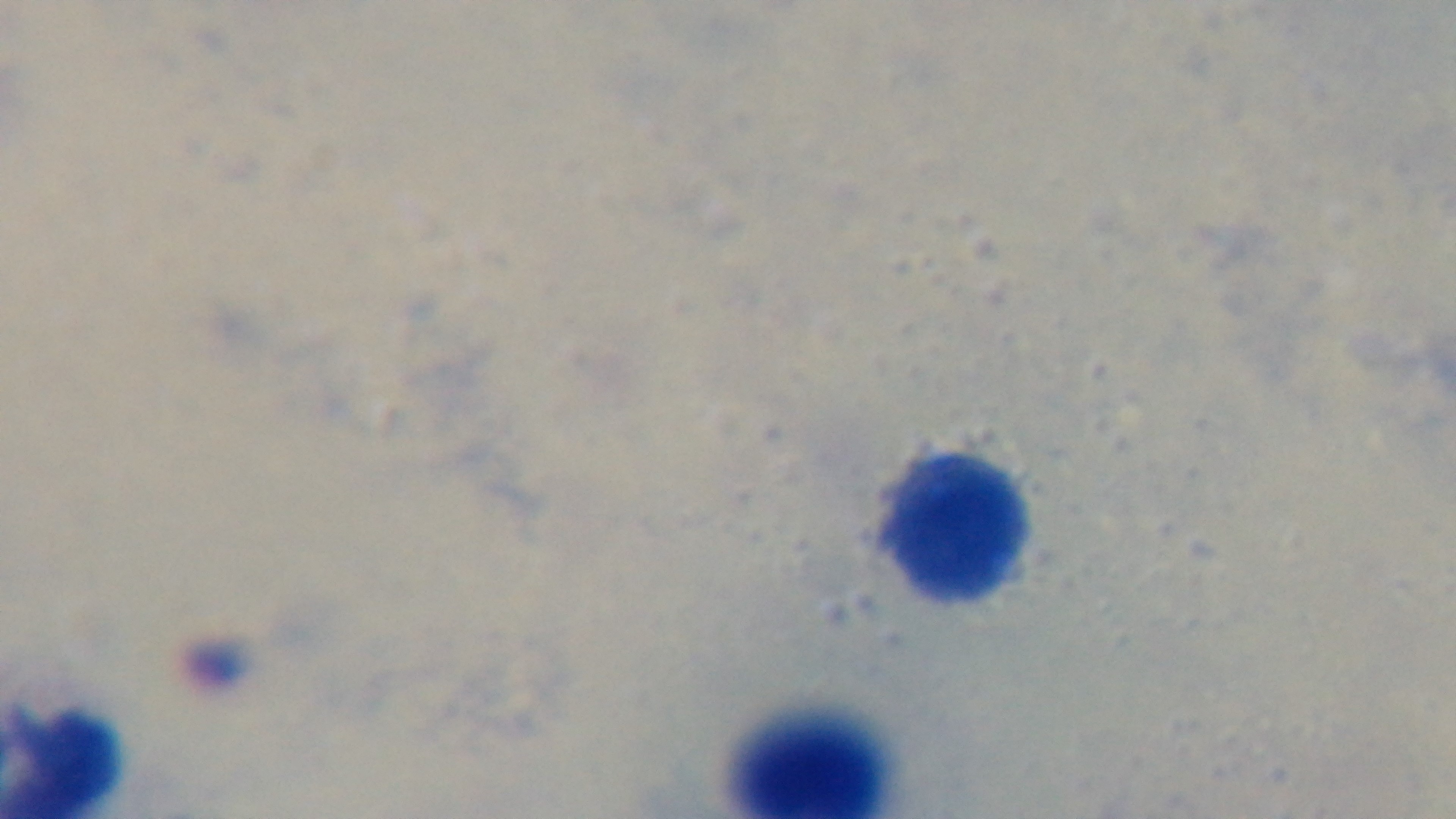

Summary:
  - Field of view: single
  - Capture: mounted 4K digital camera
  - Preparation: thick blood film
  - Modality: light microscopy
  - Malaria status: uninfected
  - Stain: Giemsa
  - Objective: 100x oil immersion